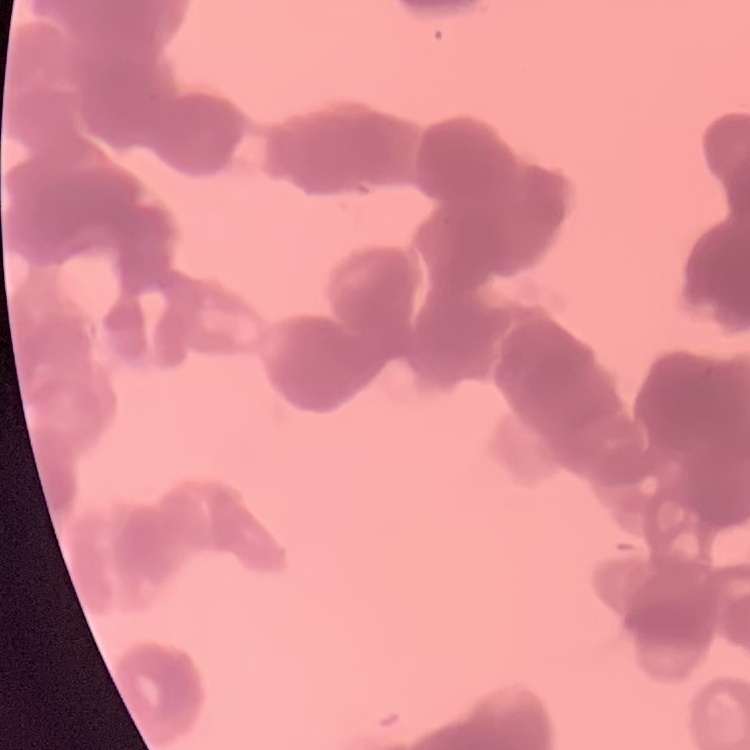
Summary:
  - Erythrocyte morphology: rouleaux formation
  - Stain: Field's or Giemsa
  - Image type: one tile cut from a larger photomicrograph
  - Preparation: thin blood smear